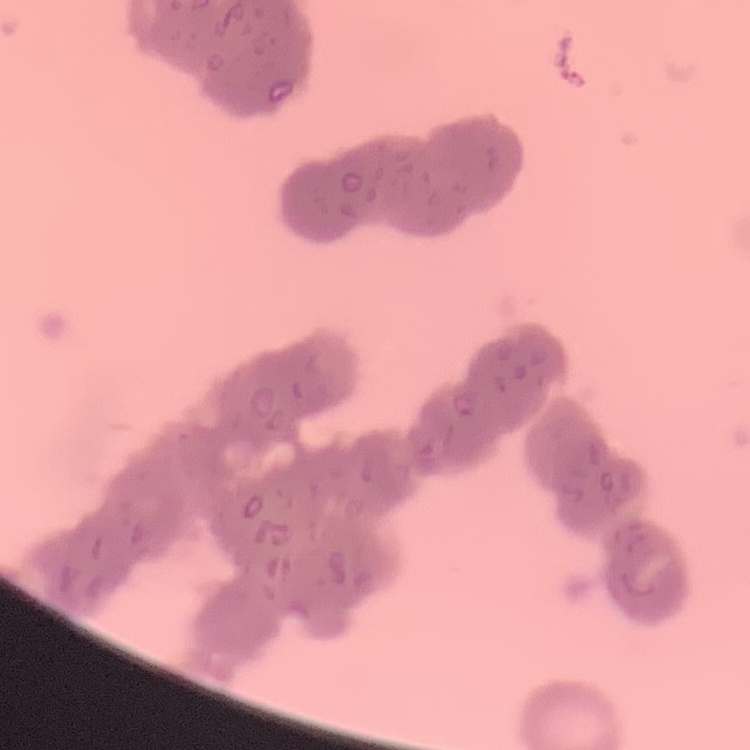

Summary:
  - Erythrocyte morphology: rouleaux formation
  - Preparation: thin blood smear
  - Image type: one tile cut from a larger photomicrograph
  - Stain: Field's or Giemsa